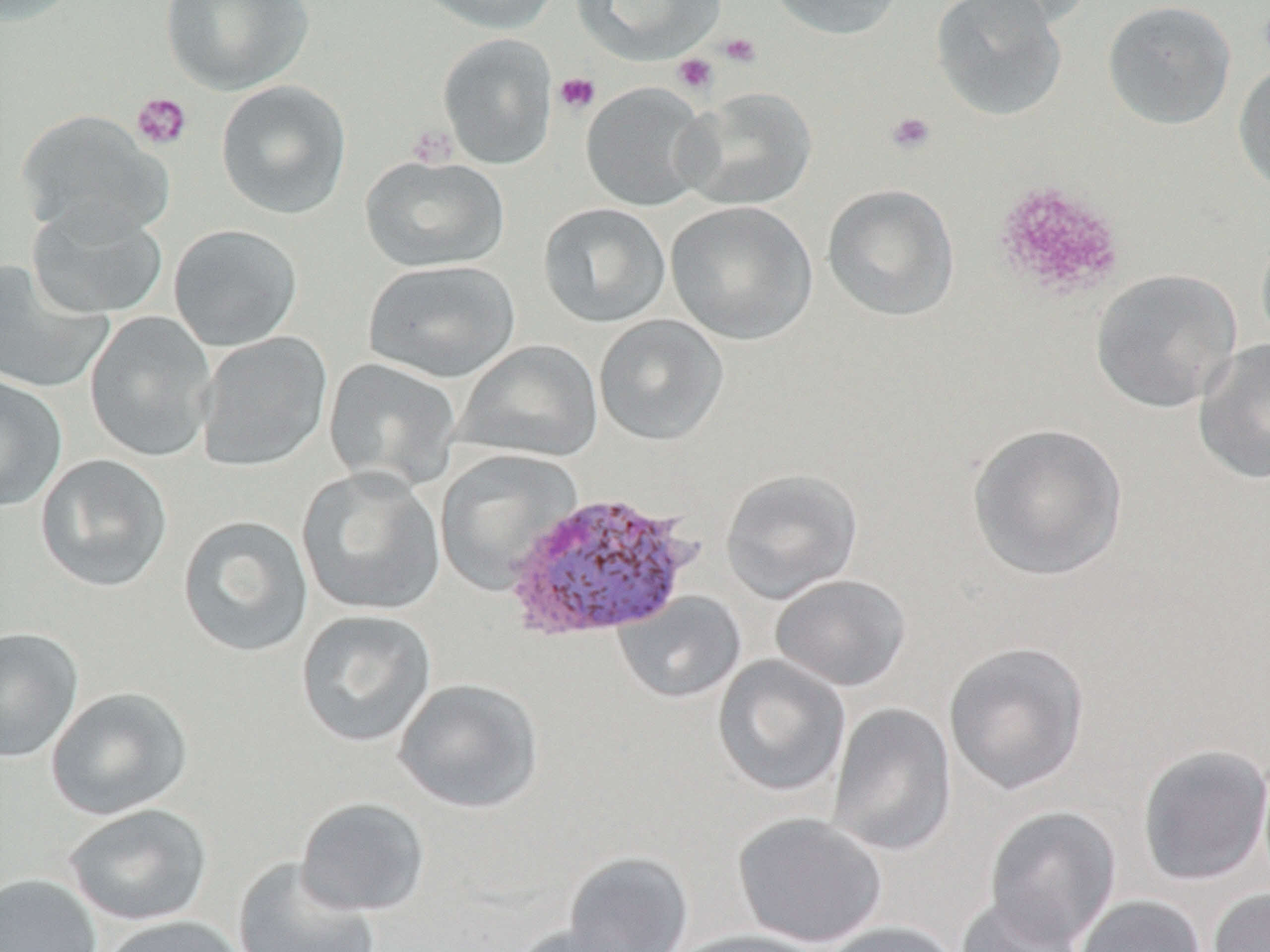
Summary:
  - Coordinate format: approximate bounding boxes as named x1/y1/x2/y2 corners in pixels
  - Plasmodium vivax-infected red blood cell locations: (x1=502, y1=491, x2=699, y2=644)
  - Uninfected red blood cell locations: (x1=0, y1=0, x2=81, y2=27), (x1=159, y1=0, x2=313, y2=95), (x1=412, y1=0, x2=560, y2=35), (x1=572, y1=0, x2=723, y2=65), (x1=766, y1=0, x2=906, y2=40), (x1=931, y1=0, x2=1067, y2=122), (x1=956, y1=0, x2=1094, y2=31), (x1=1102, y1=0, x2=1237, y2=130), (x1=437, y1=33, x2=558, y2=169), (x1=1233, y1=59, x2=1270, y2=197), (x1=215, y1=79, x2=352, y2=219), (x1=581, y1=81, x2=711, y2=212), (x1=676, y1=86, x2=817, y2=211), (x1=15, y1=109, x2=173, y2=241), (x1=360, y1=154, x2=510, y2=273), (x1=822, y1=182, x2=961, y2=322), (x1=665, y1=200, x2=817, y2=345), (x1=538, y1=202, x2=671, y2=329), (x1=26, y1=203, x2=168, y2=319), (x1=1255, y1=222, x2=1270, y2=353), (x1=168, y1=224, x2=303, y2=352), (x1=0, y1=259, x2=113, y2=395), (x1=364, y1=259, x2=521, y2=383), (x1=1090, y1=269, x2=1241, y2=413), (x1=84, y1=311, x2=216, y2=463), (x1=594, y1=314, x2=728, y2=446), (x1=196, y1=331, x2=333, y2=472), (x1=1193, y1=338, x2=1270, y2=485), (x1=454, y1=340, x2=603, y2=463), (x1=323, y1=357, x2=461, y2=489), (x1=0, y1=374, x2=68, y2=512), (x1=966, y1=422, x2=1128, y2=582), (x1=434, y1=449, x2=582, y2=595), (x1=34, y1=453, x2=174, y2=593), (x1=296, y1=466, x2=446, y2=617), (x1=719, y1=467, x2=863, y2=603), (x1=177, y1=515, x2=314, y2=657), (x1=770, y1=574, x2=912, y2=691), (x1=613, y1=590, x2=746, y2=704), (x1=295, y1=609, x2=437, y2=749), (x1=0, y1=626, x2=84, y2=764), (x1=943, y1=641, x2=1090, y2=796), (x1=712, y1=654, x2=850, y2=798), (x1=393, y1=678, x2=544, y2=813), (x1=46, y1=686, x2=194, y2=820), (x1=827, y1=702, x2=957, y2=857), (x1=1137, y1=743, x2=1270, y2=887), (x1=294, y1=797, x2=431, y2=917), (x1=63, y1=803, x2=213, y2=927), (x1=984, y1=805, x2=1122, y2=947), (x1=731, y1=812, x2=889, y2=948), (x1=563, y1=850, x2=694, y2=952), (x1=232, y1=856, x2=380, y2=952), (x1=0, y1=872, x2=102, y2=952), (x1=1207, y1=888, x2=1270, y2=952), (x1=955, y1=892, x2=1087, y2=952), (x1=1073, y1=895, x2=1207, y2=952), (x1=98, y1=914, x2=250, y2=952), (x1=816, y1=920, x2=962, y2=952), (x1=507, y1=924, x2=644, y2=952), (x1=670, y1=929, x2=831, y2=952)
  - Platelet locations: (x1=717, y1=31, x2=762, y2=68), (x1=671, y1=53, x2=718, y2=95), (x1=554, y1=71, x2=600, y2=115), (x1=131, y1=92, x2=193, y2=151), (x1=885, y1=110, x2=937, y2=156), (x1=407, y1=125, x2=458, y2=168), (x1=992, y1=179, x2=1126, y2=300)
  - Slide-level diagnosis: Plasmodium vivax
  - Magnification: 1000x
  - Image size: 1270×952 pixels
  - Preparation: thin blood smear
  - Field of view: one of a larger specimen
  - Modality: light microscopy
  - Stain: May-Grünwald-Giemsa